Name the parasite shown.
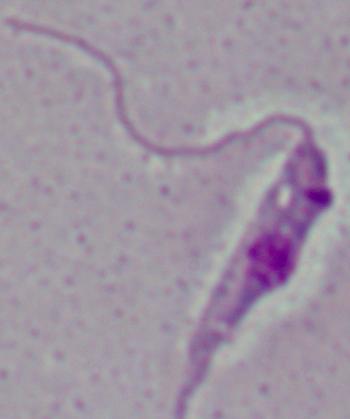
This is Leishmania.

Micrograph. Captured at 1000x magnification.